Point out each leukocyte.
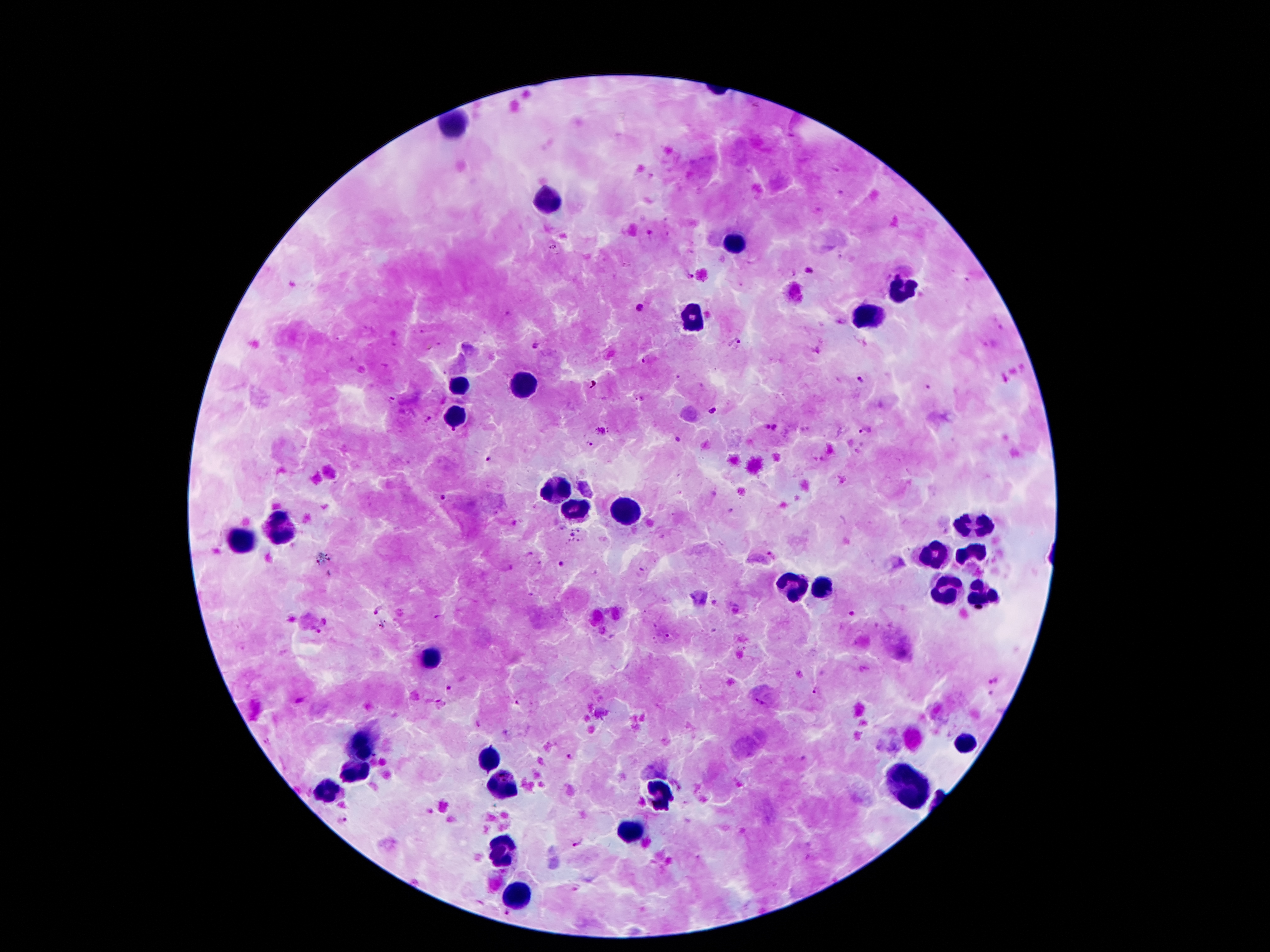
Approximate centers as (x, y) in pixels.
Leukocytes: (452, 125), (551, 197), (734, 244), (908, 291), (694, 316), (866, 318), (522, 386), (459, 388), (454, 416), (557, 492), (574, 509), (624, 513), (282, 526), (973, 528), (240, 542), (969, 553), (935, 558), (828, 585), (797, 589), (944, 589), (984, 602), (427, 658), (963, 743), (360, 749), (486, 760), (356, 772), (501, 785), (912, 789), (656, 791), (328, 795), (633, 831), (505, 849), (517, 894).

Plasmodium parasite locations: (809, 271), (689, 274), (641, 308), (737, 342), (533, 346), (859, 380), (925, 389), (712, 411), (765, 427), (775, 428), (866, 431), (590, 441), (490, 459), (444, 497), (573, 535), (561, 564), (377, 611), (853, 614), (381, 626), (993, 681), (448, 688), (817, 691), (518, 704), (570, 757), (343, 821), (579, 844), (508, 915). Patient malaria status: positive for Plasmodium falciparum. Thick peripheral-blood smear. One field from this slide. Photographed through the microscope eyepiece with a smartphone camera. Giemsa-stained preparation. Image is 1270×952 pixels. 100x magnification.